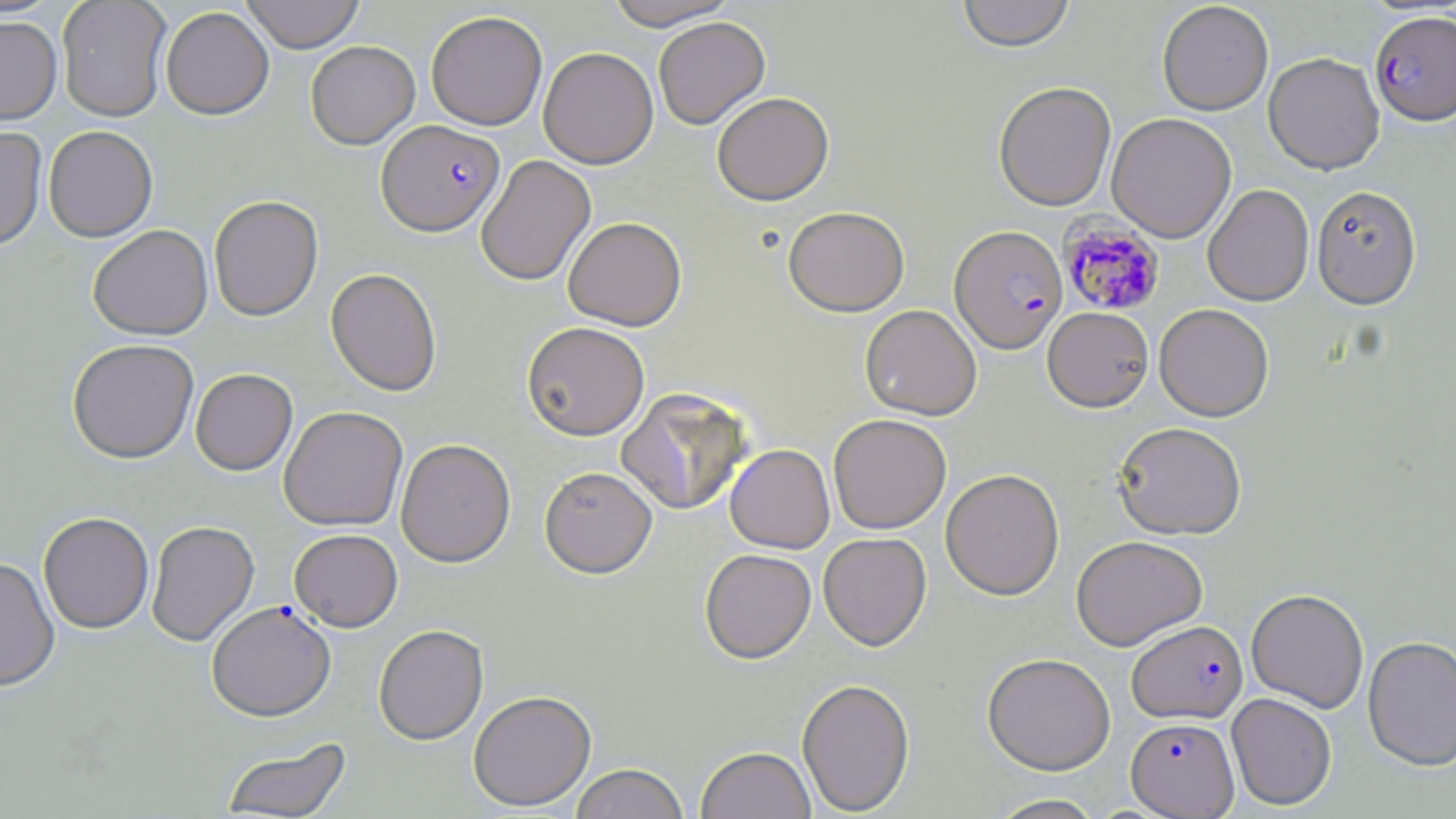 Approximate bounding boxes as (x1,y1)-(x2,y2) corner pairs in pixels. Plasmodium falciparum-infected red blood cell locations: (1370,10)-(1455,125), (377,119)-(504,236), (1060,216)-(1165,316), (950,225)-(1067,353), (206,601)-(335,722), (1127,619)-(1248,723), (1125,717)-(1239,818). Uninfected red blood cell locations: (56,0)-(172,121), (240,0)-(365,53), (604,0)-(739,30), (957,0)-(1074,52), (1157,2)-(1273,115), (161,7)-(274,120), (426,10)-(547,130), (0,16)-(62,125), (653,17)-(770,129), (305,40)-(420,149), (538,47)-(658,168), (1263,52)-(1384,174), (993,81)-(1116,211), (712,92)-(833,206), (1107,113)-(1236,243), (0,126)-(47,253), (43,126)-(158,242), (476,155)-(596,286), (1203,184)-(1314,306), (1312,186)-(1422,308), (208,196)-(323,322), (783,206)-(909,317), (563,217)-(687,330), (88,225)-(213,340), (326,269)-(442,396), (1154,303)-(1274,421), (860,304)-(982,420), (1042,307)-(1153,412), (522,321)-(649,440), (67,339)-(199,464), (190,368)-(297,475), (616,387)-(751,516), (279,406)-(408,531), (828,413)-(951,534), (1112,421)-(1247,539), (396,439)-(515,568), (725,444)-(834,553), (539,466)-(657,579), (940,468)-(1064,600), (38,512)-(154,634), (146,521)-(259,646), (289,529)-(402,631), (818,532)-(932,650), (1071,535)-(1208,650), (700,549)-(816,664), (0,558)-(60,692), (1246,588)-(1369,713), (374,626)-(489,746), (1363,635)-(1456,772), (983,653)-(1116,774), (797,679)-(915,816), (468,691)-(596,812), (1226,692)-(1337,810), (220,738)-(352,818), (696,746)-(816,819), (570,764)-(689,819), (985,794)-(1107,819). Slide-level diagnosis: Plasmodium falciparum. Light microscopy. Captured at 1000x magnification. May-Grünwald-Giemsa stain. Image is 1456×819 pixels. Single field of view. Thin blood smear.